State the blood parasite species.
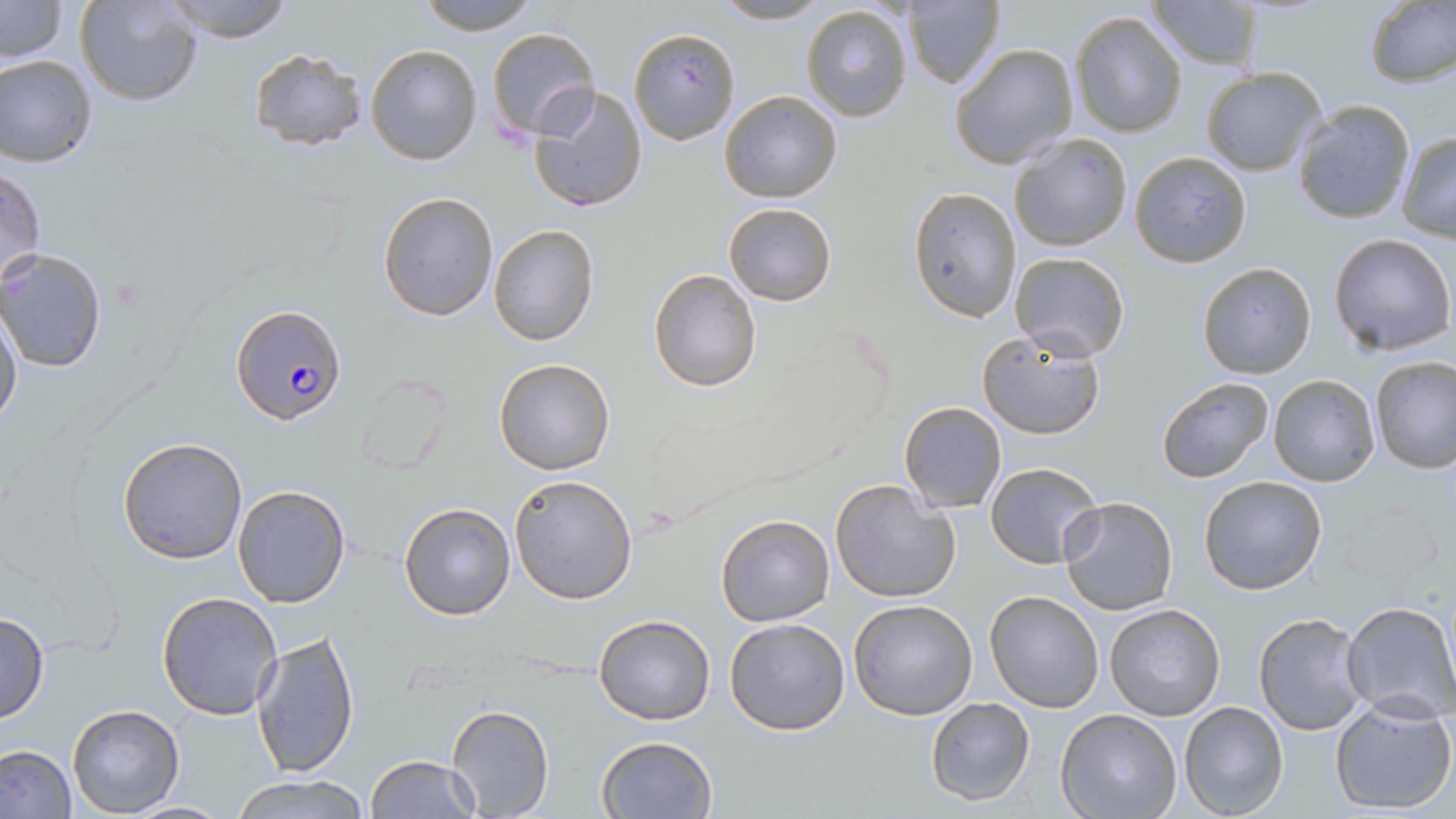

Plasmodium falciparum.

Approximate bounding boxes as named x1/y1/x2/y2 corners in pixels. Plasmodium falciparum-infected red blood cell locations: (x1=231, y1=300, x2=346, y2=423). Uninfected red blood cell locations: (x1=0, y1=0, x2=68, y2=64), (x1=74, y1=0, x2=203, y2=107), (x1=164, y1=0, x2=297, y2=44), (x1=416, y1=0, x2=543, y2=35), (x1=1148, y1=0, x2=1267, y2=70), (x1=1364, y1=0, x2=1455, y2=89), (x1=710, y1=1, x2=831, y2=26), (x1=901, y1=1, x2=1007, y2=90), (x1=800, y1=4, x2=914, y2=123), (x1=1069, y1=9, x2=1188, y2=139), (x1=628, y1=26, x2=742, y2=145), (x1=485, y1=28, x2=601, y2=144), (x1=948, y1=42, x2=1078, y2=170), (x1=366, y1=45, x2=482, y2=165), (x1=249, y1=48, x2=367, y2=153), (x1=0, y1=54, x2=98, y2=167), (x1=1200, y1=67, x2=1327, y2=177), (x1=526, y1=82, x2=650, y2=213), (x1=719, y1=91, x2=842, y2=204), (x1=1292, y1=100, x2=1417, y2=225), (x1=1009, y1=132, x2=1132, y2=252), (x1=1396, y1=132, x2=1456, y2=242), (x1=1129, y1=151, x2=1252, y2=267), (x1=2, y1=164, x2=46, y2=287), (x1=908, y1=186, x2=1023, y2=323), (x1=377, y1=191, x2=499, y2=322), (x1=723, y1=202, x2=836, y2=307), (x1=488, y1=224, x2=598, y2=347), (x1=1328, y1=233, x2=1454, y2=356), (x1=0, y1=248, x2=107, y2=372), (x1=1009, y1=251, x2=1129, y2=362), (x1=1198, y1=261, x2=1316, y2=378), (x1=647, y1=268, x2=762, y2=392), (x1=0, y1=304, x2=23, y2=433), (x1=977, y1=328, x2=1107, y2=440), (x1=493, y1=357, x2=618, y2=476), (x1=1369, y1=357, x2=1456, y2=474), (x1=352, y1=370, x2=455, y2=476), (x1=1267, y1=374, x2=1380, y2=488), (x1=1155, y1=377, x2=1273, y2=484), (x1=899, y1=401, x2=1006, y2=514), (x1=117, y1=436, x2=248, y2=565), (x1=984, y1=461, x2=1104, y2=568), (x1=1198, y1=474, x2=1328, y2=594), (x1=509, y1=475, x2=639, y2=606), (x1=830, y1=478, x2=963, y2=605), (x1=231, y1=485, x2=352, y2=608), (x1=1058, y1=496, x2=1179, y2=617), (x1=398, y1=501, x2=518, y2=620), (x1=715, y1=513, x2=835, y2=626), (x1=156, y1=591, x2=284, y2=721), (x1=985, y1=591, x2=1104, y2=712), (x1=848, y1=598, x2=979, y2=720), (x1=1341, y1=602, x2=1456, y2=722), (x1=1104, y1=603, x2=1225, y2=722), (x1=0, y1=611, x2=49, y2=724), (x1=1252, y1=611, x2=1369, y2=737), (x1=592, y1=612, x2=717, y2=725), (x1=724, y1=617, x2=852, y2=736), (x1=251, y1=630, x2=359, y2=777), (x1=924, y1=697, x2=1035, y2=806), (x1=1328, y1=698, x2=1456, y2=814), (x1=1178, y1=701, x2=1289, y2=819), (x1=446, y1=704, x2=555, y2=818), (x1=66, y1=705, x2=184, y2=817), (x1=1055, y1=709, x2=1183, y2=819), (x1=595, y1=734, x2=718, y2=819), (x1=0, y1=744, x2=76, y2=819), (x1=365, y1=753, x2=479, y2=818), (x1=231, y1=773, x2=371, y2=819), (x1=116, y1=799, x2=236, y2=816). Image is 1456×819 pixels. Light microscopy. May-Grünwald-Giemsa stain. 1000x magnification. Thin blood smear. Single field of view.